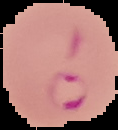
result = Plasmodium parasites identified
preparation = thin blood film
image type = cell region segmented out of the field of view; surrounding area masked to black
image size = 118×130 pixels